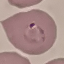
{
  "result": "malaria parasites identified",
  "capture": "smartphone camera at the microscope eyepiece",
  "image_type": "cell patch, automatically extracted from a larger field of view and resized to 64 × 64 pixels",
  "stain": "Giemsa",
  "preparation": "thin smear"
}